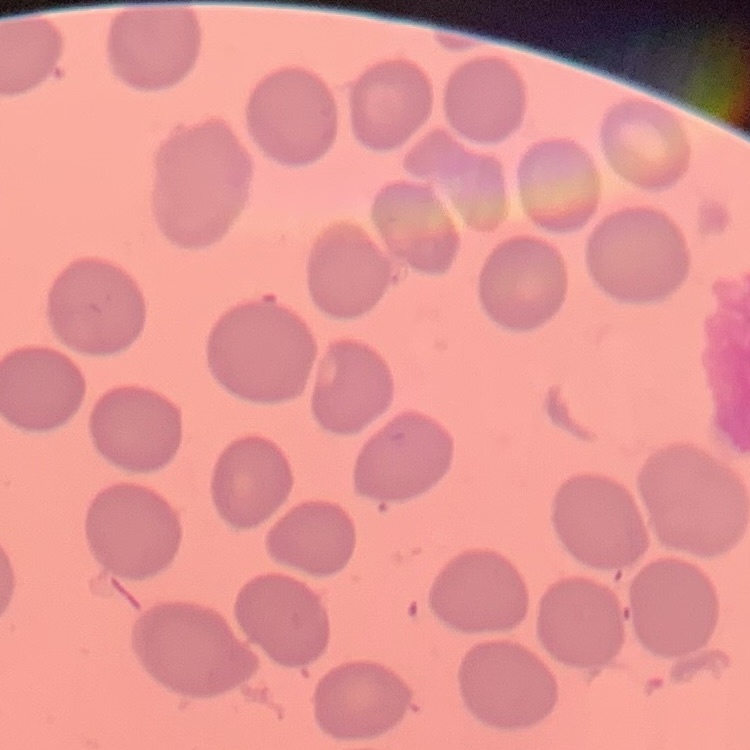
The red blood cells show no rouleaux formation. One tile cut from a larger photomicrograph. Thin blood film. Field's or Giemsa stain.